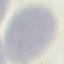

Malaria status: uninfected. Acquired by smartphone through the microscope eyepiece. Giemsa stain. Thin blood film. Cell patch, automatically extracted from a larger field of view and resized to 64 × 64 pixels.